Locate every blood parasite and identify its species.
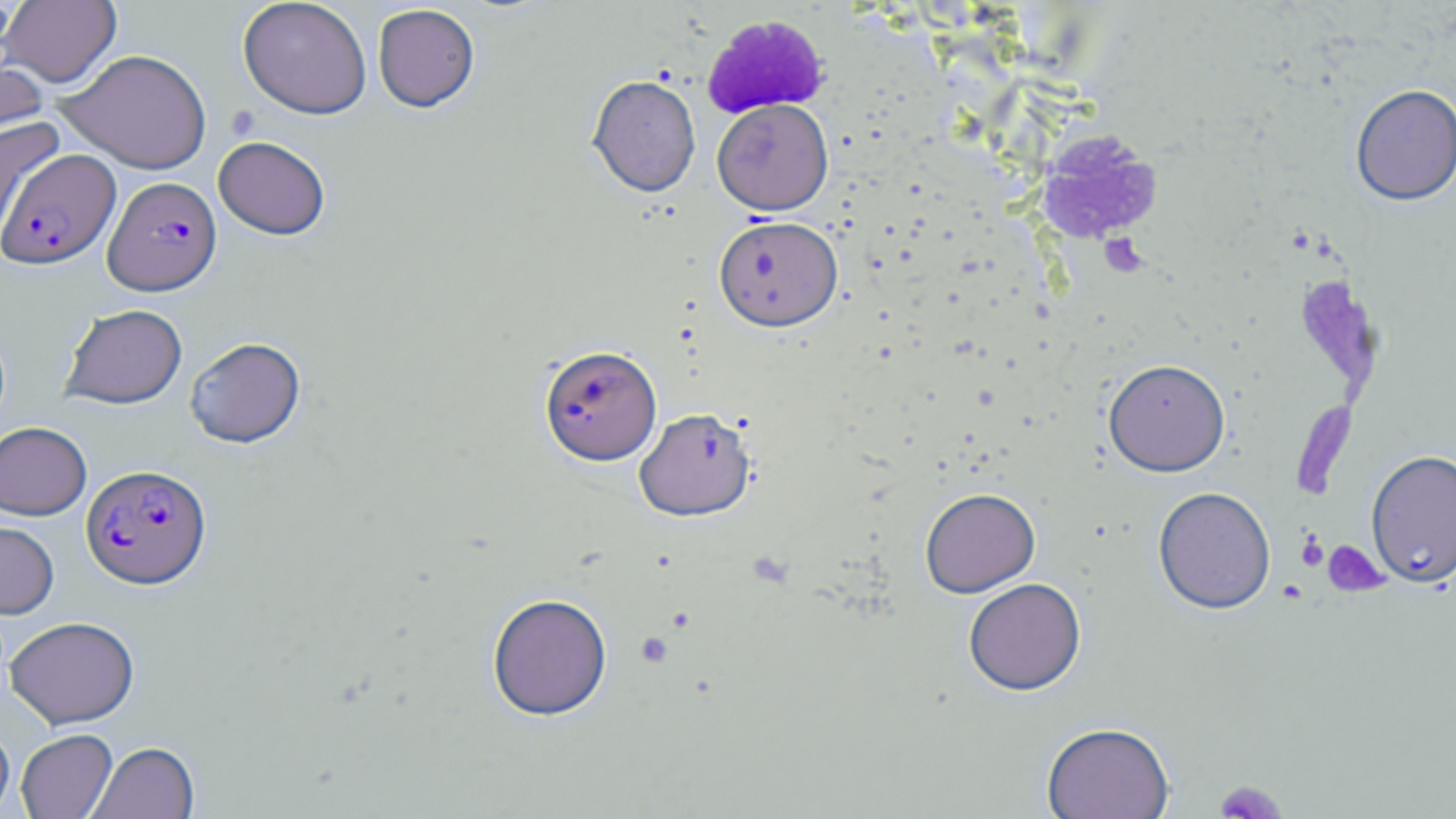
Approximate bounding boxes as named x1/y1/x2/y2 corners in pixels.
Plasmodium falciparum-infected red blood cells: (x1=0, y1=148, x2=121, y2=270), (x1=103, y1=176, x2=222, y2=295), (x1=538, y1=344, x2=662, y2=465), (x1=81, y1=463, x2=211, y2=589).
No Plasmodium ovale, Plasmodium malariae, Plasmodium vivax, Babesia divergens, or Trypanosoma brucei observed.

Uninfected red blood cell locations: (x1=238, y1=0, x2=372, y2=119), (x1=1, y1=1, x2=122, y2=88), (x1=372, y1=4, x2=480, y2=112), (x1=0, y1=47, x2=49, y2=155), (x1=58, y1=48, x2=212, y2=174), (x1=587, y1=74, x2=701, y2=198), (x1=1350, y1=86, x2=1456, y2=208), (x1=713, y1=98, x2=834, y2=215), (x1=0, y1=117, x2=61, y2=215), (x1=213, y1=135, x2=331, y2=240), (x1=714, y1=215, x2=843, y2=331), (x1=59, y1=303, x2=188, y2=409), (x1=185, y1=336, x2=306, y2=448), (x1=1103, y1=358, x2=1231, y2=477), (x1=634, y1=406, x2=757, y2=521), (x1=0, y1=421, x2=92, y2=520), (x1=1366, y1=450, x2=1456, y2=589), (x1=1152, y1=486, x2=1276, y2=615), (x1=920, y1=487, x2=1040, y2=597), (x1=0, y1=521, x2=59, y2=618), (x1=963, y1=577, x2=1086, y2=695), (x1=487, y1=592, x2=613, y2=720), (x1=4, y1=615, x2=139, y2=729), (x1=1041, y1=721, x2=1175, y2=819), (x1=0, y1=722, x2=15, y2=817), (x1=16, y1=728, x2=117, y2=819), (x1=88, y1=741, x2=199, y2=819). Platelet locations: (x1=226, y1=105, x2=260, y2=140), (x1=1099, y1=233, x2=1147, y2=277), (x1=1297, y1=534, x2=1329, y2=571), (x1=1323, y1=540, x2=1389, y2=598), (x1=636, y1=632, x2=674, y2=668), (x1=1215, y1=779, x2=1288, y2=818). Slide-level diagnosis: Plasmodium falciparum. May-Grünwald-Giemsa-stained preparation. Thin blood smear. Captured at 1000x magnification. Image is 1456×819 pixels. Single field of view. Light microscopy.